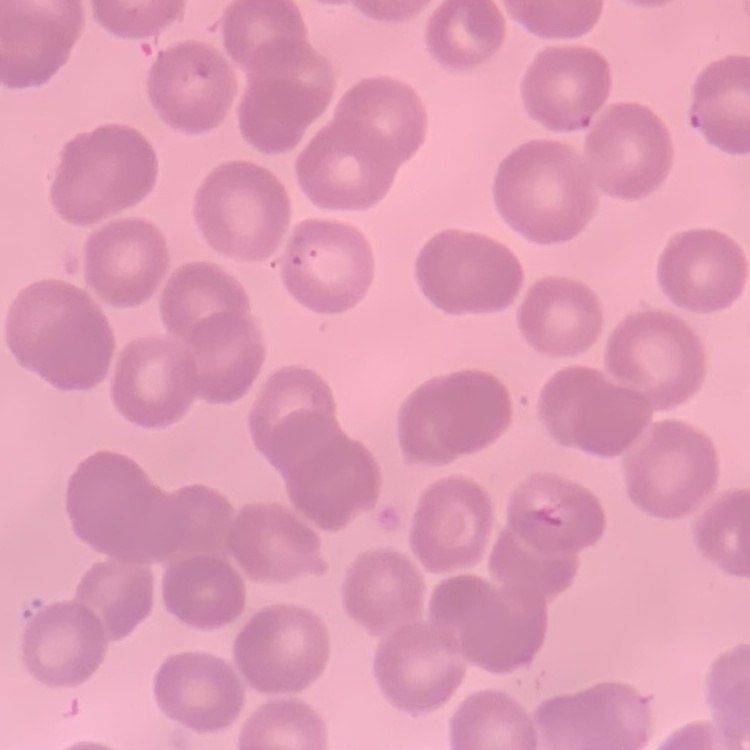
Summary:
  - Red blood cell morphology: no rouleaux formation
  - Stain: Field's or Giemsa
  - Preparation: thin blood film
  - Image type: square crop of a larger photomicrograph